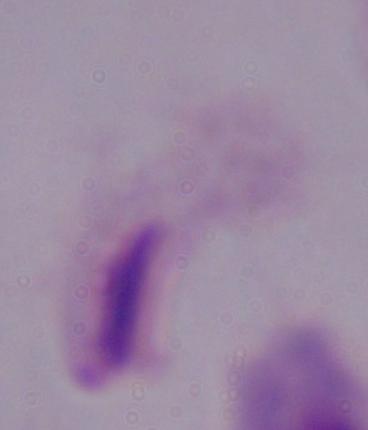

Summary:
  - Magnification: 1000x
  - Modality: micrograph
  - Identification: trichomonad